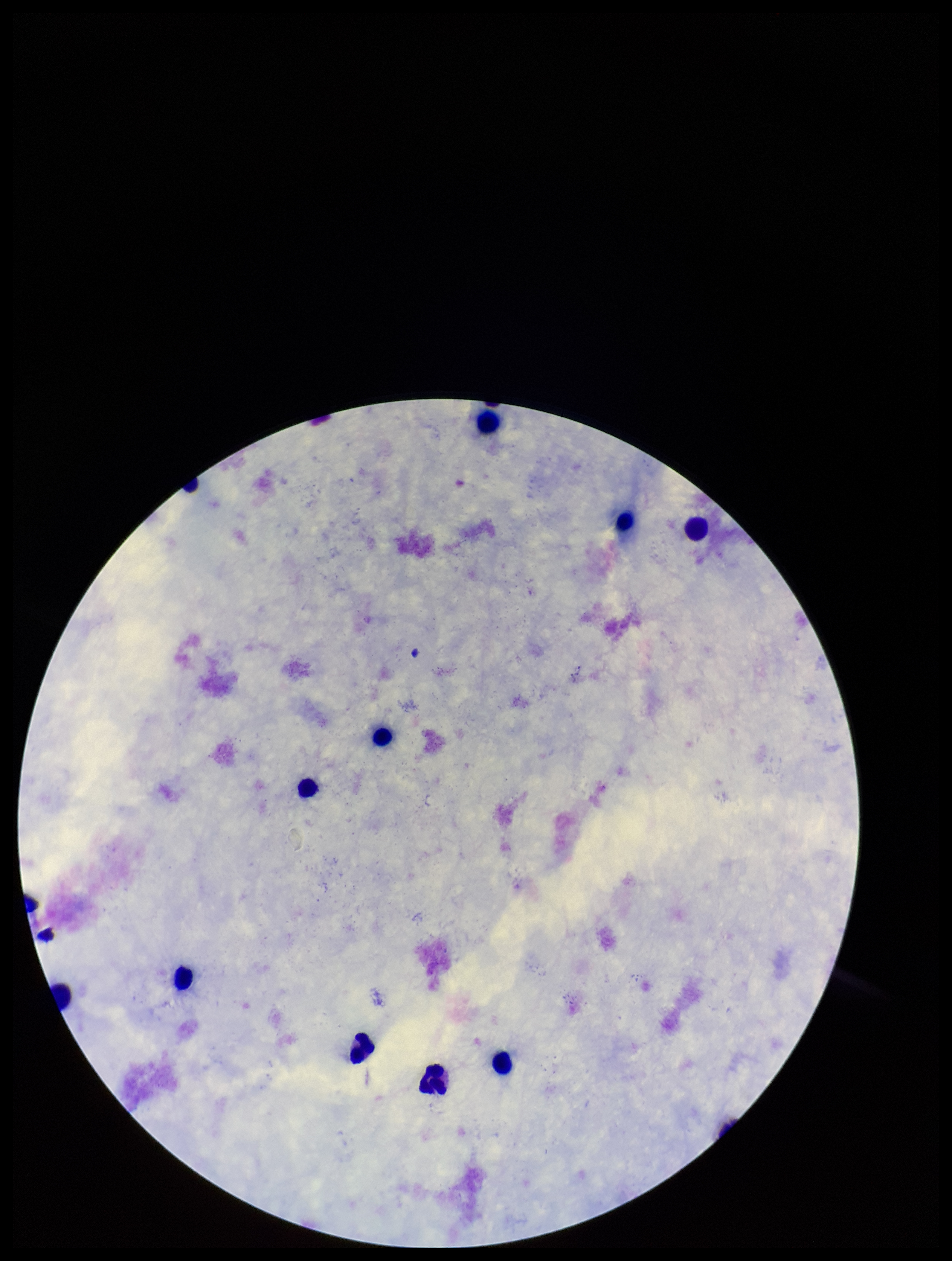

leukocyte_count: 10
parasite_count: 0
stain: Giemsa
field_of_view: single
plasmodium_parasites: none seen
preparation: thick
capture: smartphone photograph through the microscope eyepiece
patient_malaria_status: negative
image_size: 952×1261 pixels